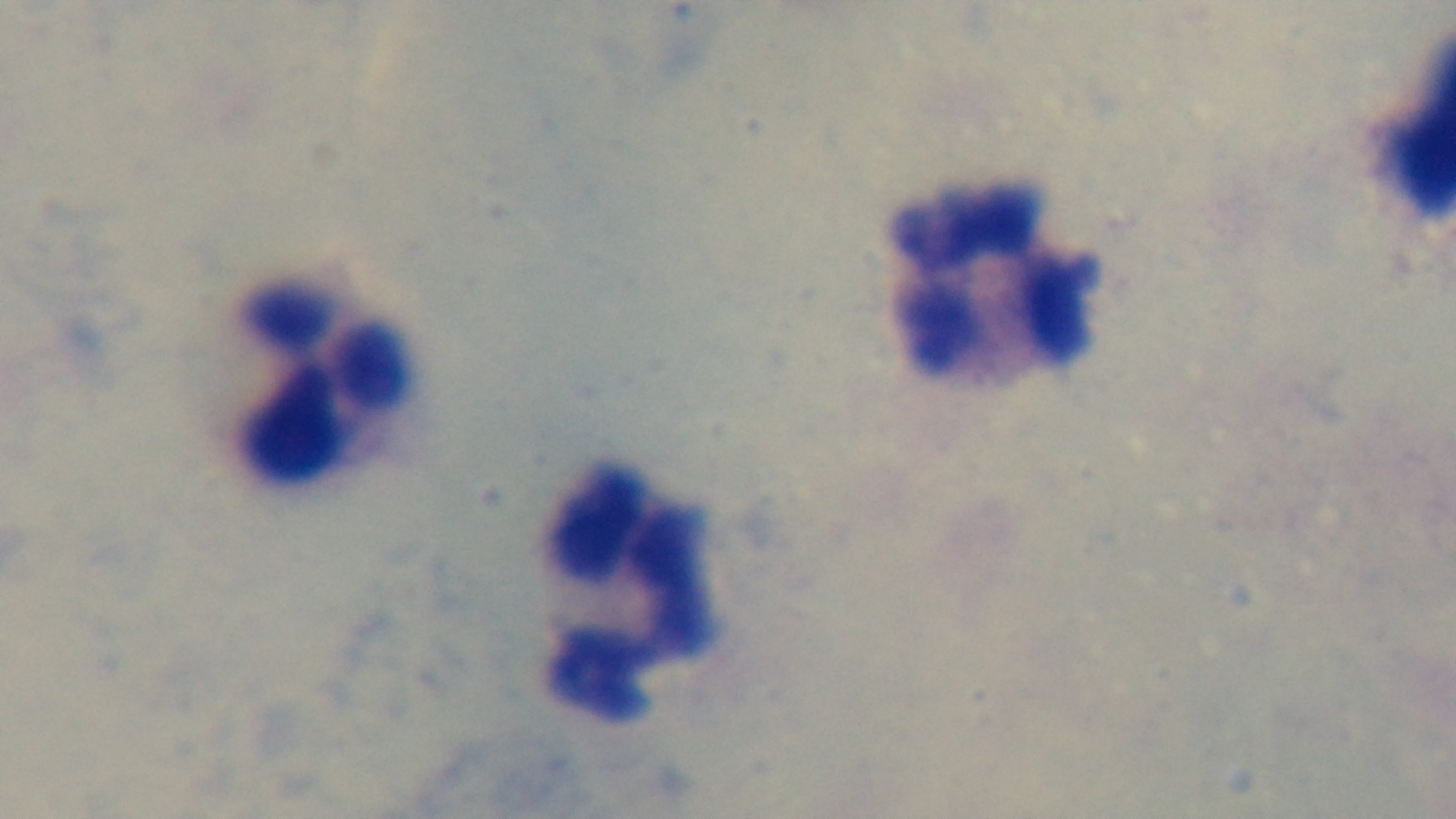
{
  "objective": "100x oil immersion",
  "capture": "mounted 4K digital camera",
  "preparation": "thick smear",
  "field_of_view": "one from the slide",
  "stain": "Giemsa",
  "modality": "light microscopy",
  "malaria_status": "negative"
}